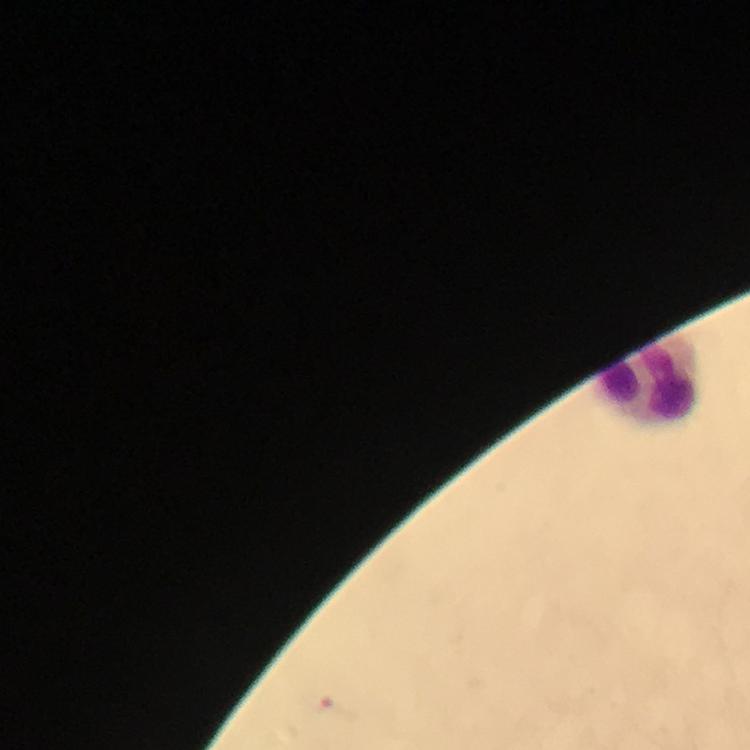

Approximate object centers, in pixels from the top-left corner.
Summary:
  - Leukocyte locations: (x=648, y=382)
  - Malaria parasite locations: (x=317, y=699)
  - Magnification: 100x
  - Preparation: thick blood film
  - Context: from a malaria diagnostic workup
  - Image size: 750×750 pixels
  - Immersion oil: used
  - Capture: smartphone photograph through a microscope
  - Stain: Giemsa
  - Cropped from: a single field of view